Outline each blood parasite and name the species.
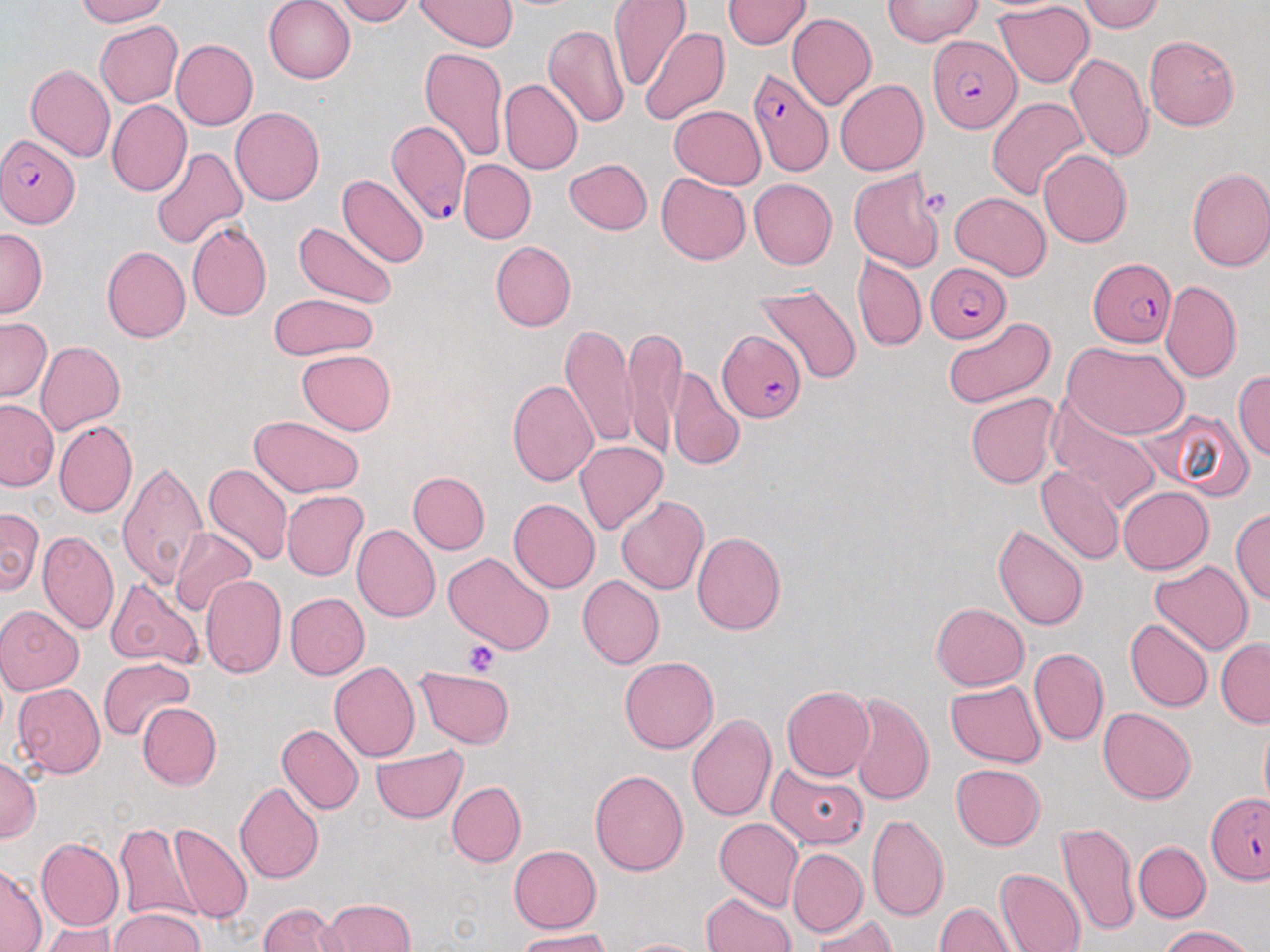
Approximate bounding boxes as named x1/y1/x2/y2 corners in pixels.
Plasmodium falciparum-infected red blood cells: (x1=927, y1=33, x2=1020, y2=133), (x1=747, y1=68, x2=834, y2=177), (x1=384, y1=117, x2=468, y2=230), (x1=0, y1=135, x2=80, y2=228), (x1=1089, y1=256, x2=1177, y2=346), (x1=925, y1=261, x2=1011, y2=342), (x1=718, y1=330, x2=805, y2=420), (x1=1208, y1=794, x2=1270, y2=882).
No Plasmodium ovale, Plasmodium malariae, Plasmodium vivax, Babesia divergens, or Trypanosoma brucei observed.

slide_level_diagnosis: Plasmodium falciparum
stain: May-Grünwald-Giemsa
image_size: 1270×952 pixels
uninfected_red_blood_cell_locations: 'approximate bounding boxes as named x1/y1/x2/y2 corners in pixels: (x1=74, y1=0, x2=170, y2=26), (x1=264, y1=0, x2=356, y2=83), (x1=334, y1=0, x2=416, y2=25), (x1=415, y1=0, x2=516, y2=51), (x1=609, y1=0, x2=691, y2=92), (x1=723, y1=0, x2=810, y2=49), (x1=882, y1=0, x2=983, y2=46), (x1=1077, y1=0, x2=1167, y2=32), (x1=993, y1=2, x2=1095, y2=87), (x1=788, y1=13, x2=877, y2=110), (x1=95, y1=21, x2=183, y2=106), (x1=543, y1=23, x2=629, y2=128), (x1=641, y1=26, x2=729, y2=126), (x1=1144, y1=35, x2=1239, y2=130), (x1=171, y1=39, x2=258, y2=130), (x1=418, y1=46, x2=509, y2=162), (x1=1066, y1=52, x2=1154, y2=160), (x1=25, y1=65, x2=114, y2=163), (x1=498, y1=79, x2=583, y2=173), (x1=836, y1=79, x2=929, y2=176), (x1=987, y1=96, x2=1089, y2=200), (x1=107, y1=100, x2=191, y2=196), (x1=230, y1=106, x2=324, y2=206), (x1=669, y1=106, x2=766, y2=189), (x1=150, y1=146, x2=247, y2=250), (x1=1038, y1=148, x2=1132, y2=248), (x1=564, y1=158, x2=652, y2=234), (x1=458, y1=159, x2=535, y2=243), (x1=1185, y1=166, x2=1270, y2=272), (x1=849, y1=168, x2=945, y2=273), (x1=657, y1=173, x2=750, y2=264), (x1=337, y1=175, x2=429, y2=267), (x1=748, y1=178, x2=838, y2=270), (x1=951, y1=192, x2=1051, y2=280), (x1=186, y1=221, x2=271, y2=322), (x1=292, y1=221, x2=397, y2=310), (x1=0, y1=229, x2=48, y2=318), (x1=490, y1=240, x2=576, y2=331), (x1=101, y1=246, x2=191, y2=342), (x1=853, y1=256, x2=926, y2=352), (x1=1160, y1=280, x2=1243, y2=383), (x1=755, y1=281, x2=862, y2=386), (x1=268, y1=293, x2=379, y2=359), (x1=944, y1=316, x2=1055, y2=409), (x1=0, y1=318, x2=51, y2=401), (x1=561, y1=324, x2=636, y2=448), (x1=622, y1=327, x2=683, y2=460), (x1=35, y1=340, x2=126, y2=436), (x1=1064, y1=341, x2=1189, y2=440), (x1=296, y1=349, x2=396, y2=435), (x1=668, y1=366, x2=745, y2=472), (x1=1233, y1=369, x2=1270, y2=463), (x1=507, y1=379, x2=598, y2=486), (x1=965, y1=393, x2=1060, y2=489), (x1=1046, y1=398, x2=1161, y2=515), (x1=0, y1=399, x2=58, y2=491), (x1=1150, y1=409, x2=1254, y2=499), (x1=250, y1=416, x2=365, y2=497), (x1=54, y1=421, x2=137, y2=518), (x1=574, y1=441, x2=667, y2=534), (x1=117, y1=460, x2=210, y2=590), (x1=204, y1=462, x2=293, y2=566), (x1=1036, y1=464, x2=1125, y2=565), (x1=407, y1=471, x2=489, y2=554), (x1=1117, y1=486, x2=1213, y2=574), (x1=281, y1=491, x2=368, y2=580), (x1=616, y1=495, x2=709, y2=595), (x1=508, y1=498, x2=601, y2=592), (x1=0, y1=507, x2=43, y2=595), (x1=1230, y1=507, x2=1270, y2=606), (x1=993, y1=523, x2=1089, y2=630), (x1=352, y1=524, x2=440, y2=622), (x1=169, y1=529, x2=257, y2=619), (x1=37, y1=530, x2=119, y2=635), (x1=691, y1=532, x2=786, y2=634), (x1=443, y1=551, x2=556, y2=655), (x1=1150, y1=559, x2=1254, y2=654), (x1=200, y1=574, x2=287, y2=678), (x1=577, y1=574, x2=665, y2=669), (x1=104, y1=578, x2=203, y2=669), (x1=285, y1=593, x2=369, y2=680), (x1=930, y1=602, x2=1030, y2=690), (x1=0, y1=605, x2=84, y2=695), (x1=1125, y1=619, x2=1213, y2=712), (x1=1216, y1=638, x2=1270, y2=728), (x1=1029, y1=648, x2=1109, y2=746), (x1=620, y1=656, x2=719, y2=754), (x1=97, y1=658, x2=194, y2=740), (x1=330, y1=661, x2=420, y2=761), (x1=415, y1=666, x2=514, y2=749), (x1=946, y1=679, x2=1045, y2=768), (x1=13, y1=683, x2=106, y2=778), (x1=782, y1=685, x2=874, y2=781), (x1=848, y1=692, x2=934, y2=806), (x1=136, y1=702, x2=221, y2=790), (x1=1099, y1=708, x2=1196, y2=804), (x1=687, y1=713, x2=777, y2=821), (x1=1259, y1=719, x2=1270, y2=813), (x1=277, y1=723, x2=364, y2=814), (x1=371, y1=745, x2=468, y2=823), (x1=0, y1=756, x2=40, y2=843), (x1=770, y1=762, x2=866, y2=851), (x1=951, y1=763, x2=1046, y2=850), (x1=590, y1=769, x2=688, y2=874), (x1=234, y1=781, x2=325, y2=884), (x1=447, y1=782, x2=525, y2=866), (x1=866, y1=813, x2=950, y2=923), (x1=714, y1=818, x2=803, y2=912), (x1=1057, y1=820, x2=1139, y2=940), (x1=113, y1=821, x2=205, y2=927), (x1=169, y1=822, x2=252, y2=926), (x1=36, y1=838, x2=125, y2=931), (x1=1132, y1=841, x2=1210, y2=922), (x1=509, y1=844, x2=601, y2=932), (x1=788, y1=847, x2=867, y2=937), (x1=0, y1=864, x2=45, y2=951), (x1=993, y1=866, x2=1085, y2=952), (x1=702, y1=891, x2=796, y2=952), (x1=318, y1=898, x2=416, y2=952), (x1=258, y1=903, x2=348, y2=952), (x1=933, y1=903, x2=1018, y2=951), (x1=110, y1=908, x2=204, y2=952), (x1=813, y1=916, x2=898, y2=952), (x1=40, y1=922, x2=118, y2=951), (x1=1157, y1=925, x2=1253, y2=952), (x1=515, y1=929, x2=614, y2=952), (x1=618, y1=937, x2=710, y2=952)'
magnification: 1000x
modality: optical microscopy
platelet_locations: 'approximate bounding boxes as named x1/y1/x2/y2 corners in pixels: (x1=916, y1=186, x2=952, y2=220), (x1=463, y1=640, x2=499, y2=676)'
field_of_view: one of a larger specimen
preparation: thin blood film